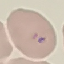 Result: malaria parasites identified. Giemsa stain. Acquired by smartphone through the microscope eyepiece. Automatically extracted cell patch, resized to 64 × 64 pixels. Thin blood smear.